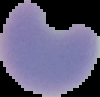

Summary:
  - Image size: 100×97 pixels
  - Image type: cell region segmented out of the field of view; surrounding area masked to black
  - Result: Plasmodium parasites identified
  - Preparation: thin blood film